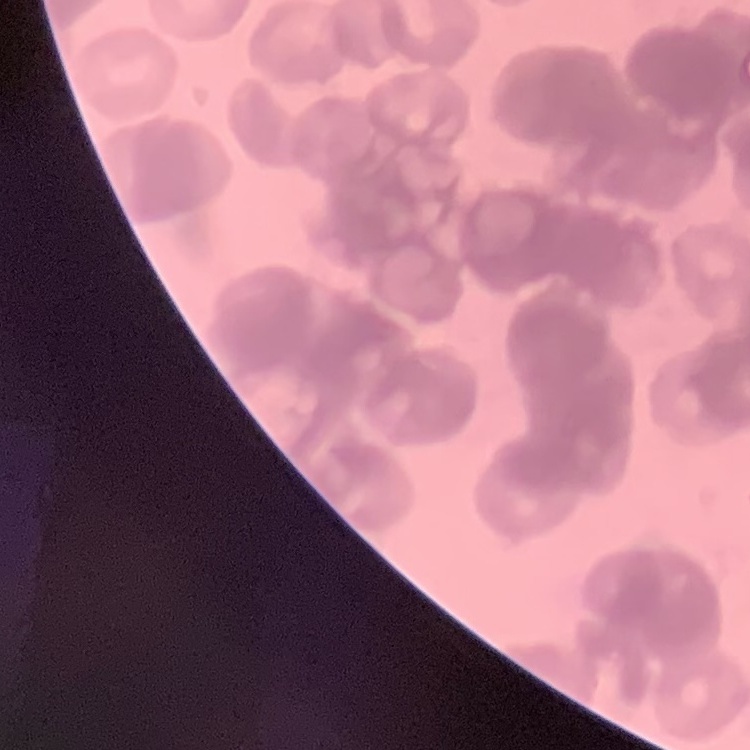

{
  "erythrocyte_morphology": "rouleaux formation",
  "stain": "Field's or Giemsa",
  "preparation": "thin blood smear",
  "image_type": "one tile cut from a larger photomicrograph"
}